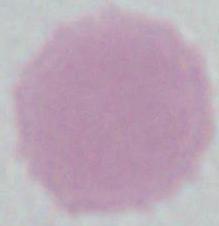
An erythrocyte is shown. Photomicrograph. 1000x magnification.